Assess this cell for malaria.
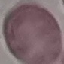

It is uninfected.

Summary:
  - Preparation: thin blood film
  - Capture: smartphone through the microscope eyepiece
  - Image type: cell patch, automatically extracted from a larger field of view and resized to 64 × 64 pixels
  - Stain: Giemsa